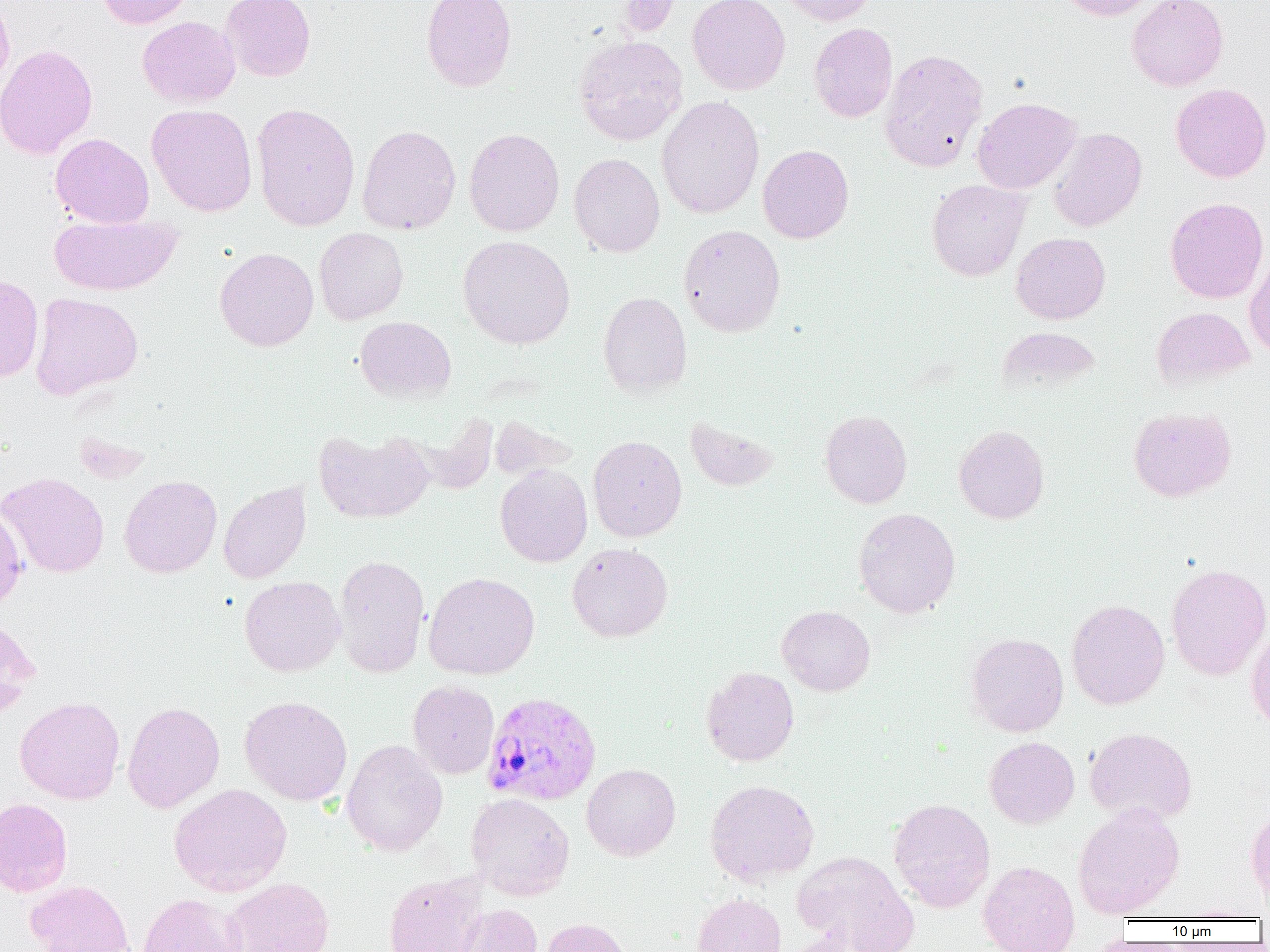

Approximate bounding boxes as (x1, y1, x2, y2) in pixels. Plasmodium vivax-infected red blood cell locations: (482, 691, 602, 807). Uninfected red blood cell locations: (95, 0, 196, 29), (219, 0, 316, 81), (421, 0, 517, 92), (615, 0, 680, 37), (688, 0, 790, 95), (779, 0, 875, 26), (1059, 0, 1162, 21), (1127, 0, 1228, 91), (0, 1, 15, 94), (137, 16, 241, 107), (809, 23, 897, 123), (573, 34, 688, 146), (0, 43, 98, 160), (879, 49, 988, 172), (1170, 83, 1270, 182), (656, 96, 764, 219), (972, 97, 1081, 194), (251, 102, 361, 232), (146, 104, 257, 217), (357, 124, 461, 235), (1048, 127, 1147, 232), (464, 128, 565, 237), (50, 133, 154, 228), (758, 144, 854, 243), (568, 153, 665, 257), (926, 179, 1030, 281), (1165, 197, 1269, 304), (49, 213, 182, 295), (678, 224, 786, 337), (314, 228, 408, 325), (1011, 233, 1110, 324), (458, 236, 575, 349), (215, 247, 319, 352), (1244, 250, 1270, 360), (0, 273, 44, 382), (598, 291, 692, 398), (30, 292, 144, 400), (1151, 307, 1255, 389), (355, 316, 456, 402), (996, 327, 1100, 395), (1128, 406, 1236, 501), (819, 409, 913, 508), (684, 415, 780, 491), (490, 416, 576, 481), (954, 425, 1049, 524), (314, 428, 434, 524), (588, 435, 687, 543), (495, 463, 593, 567), (1, 472, 109, 578), (119, 475, 222, 578), (218, 481, 311, 584), (0, 504, 27, 613), (853, 507, 961, 618), (567, 542, 673, 642), (333, 554, 430, 678), (1166, 563, 1270, 681), (423, 572, 540, 680), (239, 576, 345, 677), (1066, 599, 1170, 710), (777, 605, 875, 696), (0, 615, 41, 719), (1246, 627, 1270, 734), (965, 632, 1069, 737), (701, 666, 799, 766), (407, 680, 499, 779), (15, 695, 125, 804), (240, 696, 353, 805), (122, 701, 224, 813), (1084, 726, 1197, 825), (984, 737, 1079, 829), (341, 739, 448, 856), (582, 763, 680, 860), (704, 779, 819, 886), (169, 784, 292, 897), (466, 793, 574, 900), (0, 798, 72, 896), (888, 798, 995, 912), (1073, 803, 1184, 918), (1246, 809, 1270, 903), (792, 851, 918, 952), (977, 859, 1080, 952), (384, 873, 485, 952), (225, 877, 334, 952), (25, 879, 134, 952), (138, 893, 248, 952), (692, 893, 786, 952), (453, 903, 543, 952), (1177, 905, 1261, 921), (540, 917, 632, 952). Slide-level diagnosis: Plasmodium vivax. Captured at 1000x magnification. Thin blood film. Single field of view. Image is 1270×952 pixels. Light microscopy.